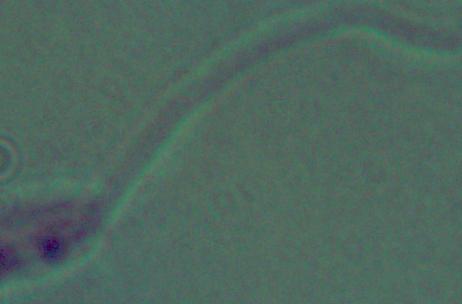

Summary:
  - Magnification: 1000x
  - Modality: micrograph
  - Identification: Leishmania